Describe the morphology of the red blood cells.
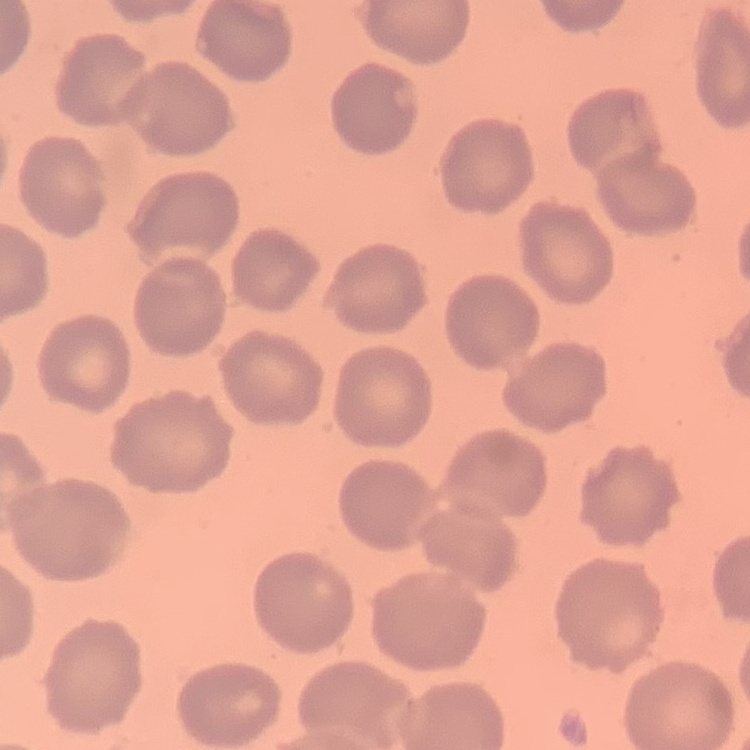

They show no rouleaux formation.

stain: Field's or Giemsa
image_type: square crop of a larger photomicrograph
preparation: thin blood smear